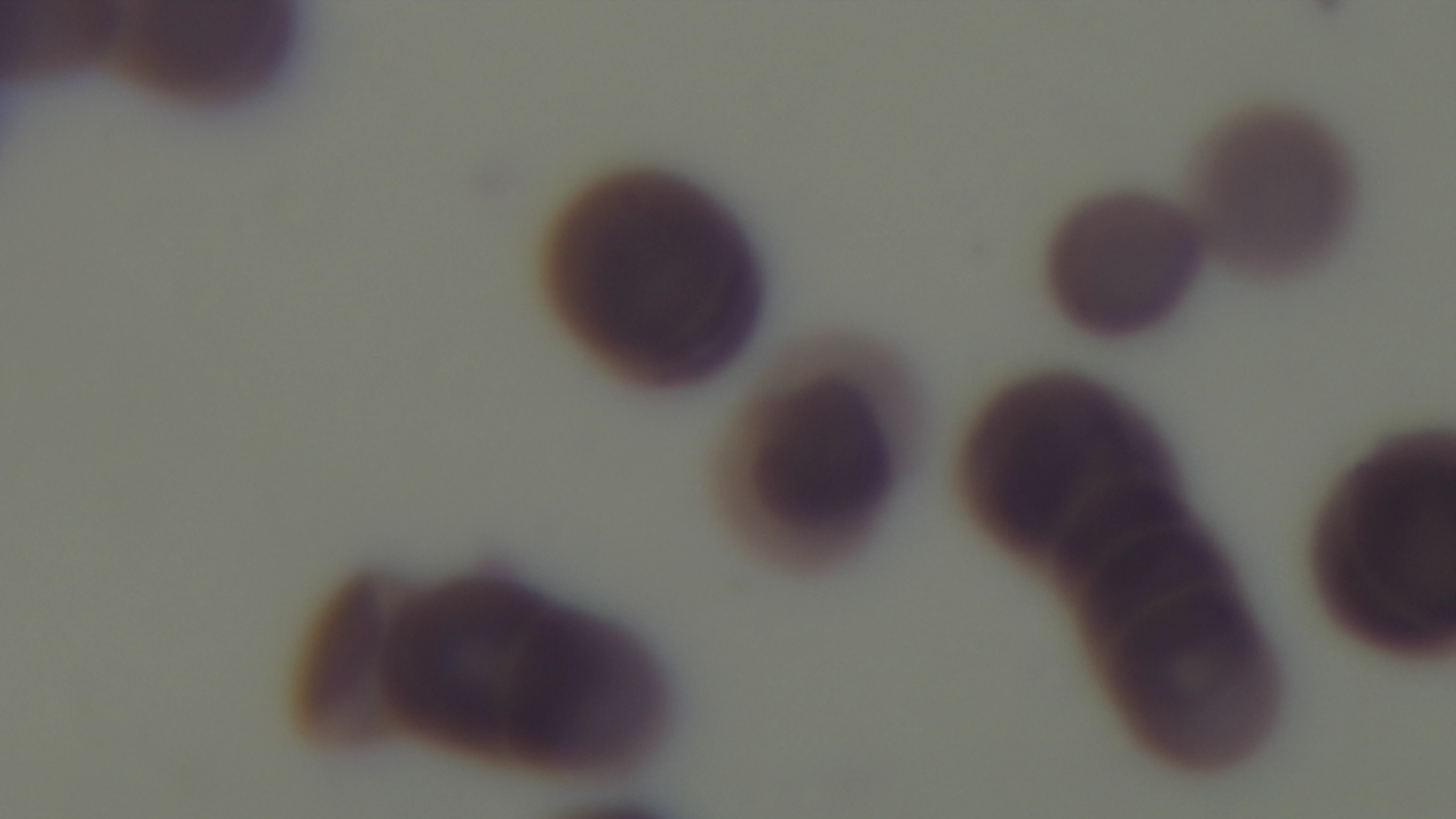
Summary:
  - Stain: Giemsa
  - Malaria status: infected
  - Objective: 100x oil immersion
  - Field of view: one from the slide
  - Capture: mounted 4K digital camera
  - Modality: light microscopy
  - Preparation: thin